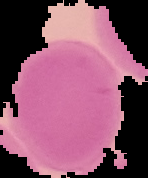

{
  "result": "no Plasmodium parasites detected",
  "image_type": "segmented cell region with the area outside set to black",
  "image_size": "148×178 pixels",
  "preparation": "thin blood film"
}